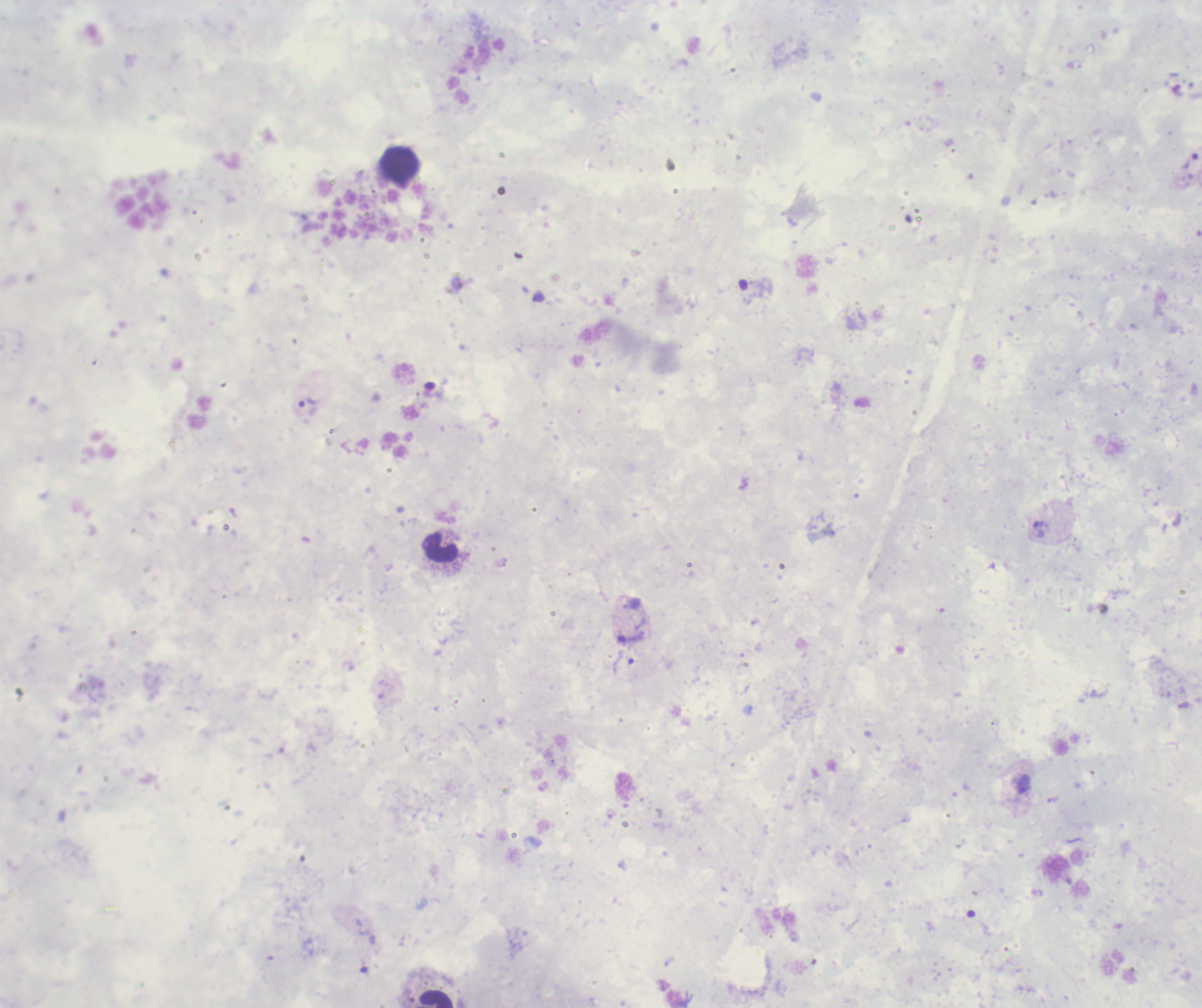

Approximate centers as {x, y} in pixels.
Summary:
  - Trophozoite locations: {1190, 162}, {308, 402}, {1038, 530}, {630, 638}
  - Leukocyte locations: {399, 164}, {441, 548}, {436, 998}
  - Stain: Romanowsky
  - Magnification: 100x
  - Image size: 1202×1008 pixels
  - Preparation: thick blood film
  - Background quality: unsatisfactory
  - Context: previously used in a real diagnosis
  - Field of view: one from this slide
  - Result: malaria parasites detected